Report the malaria status of this cell.
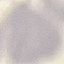

Uninfected.

Photographed with a smartphone camera at the microscope eyepiece. Giemsa stain. Thin smear of blood. Cell patch, automatically extracted from a larger field of view and resized to 64 × 64 pixels.